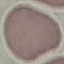

Summary:
  - Malaria status: uninfected
  - Preparation: thin smear
  - Stain: Giemsa
  - Capture: smartphone camera at the microscope eyepiece
  - Image type: cell patch, automatically extracted from a larger field of view and resized to 64 × 64 pixels